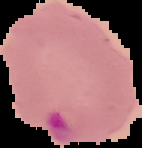
Summary:
  - Preparation: thin blood film
  - Image type: cell region segmented out of the field of view; surrounding area masked to black
  - Malaria status: parasitized
  - Image size: 142×148 pixels